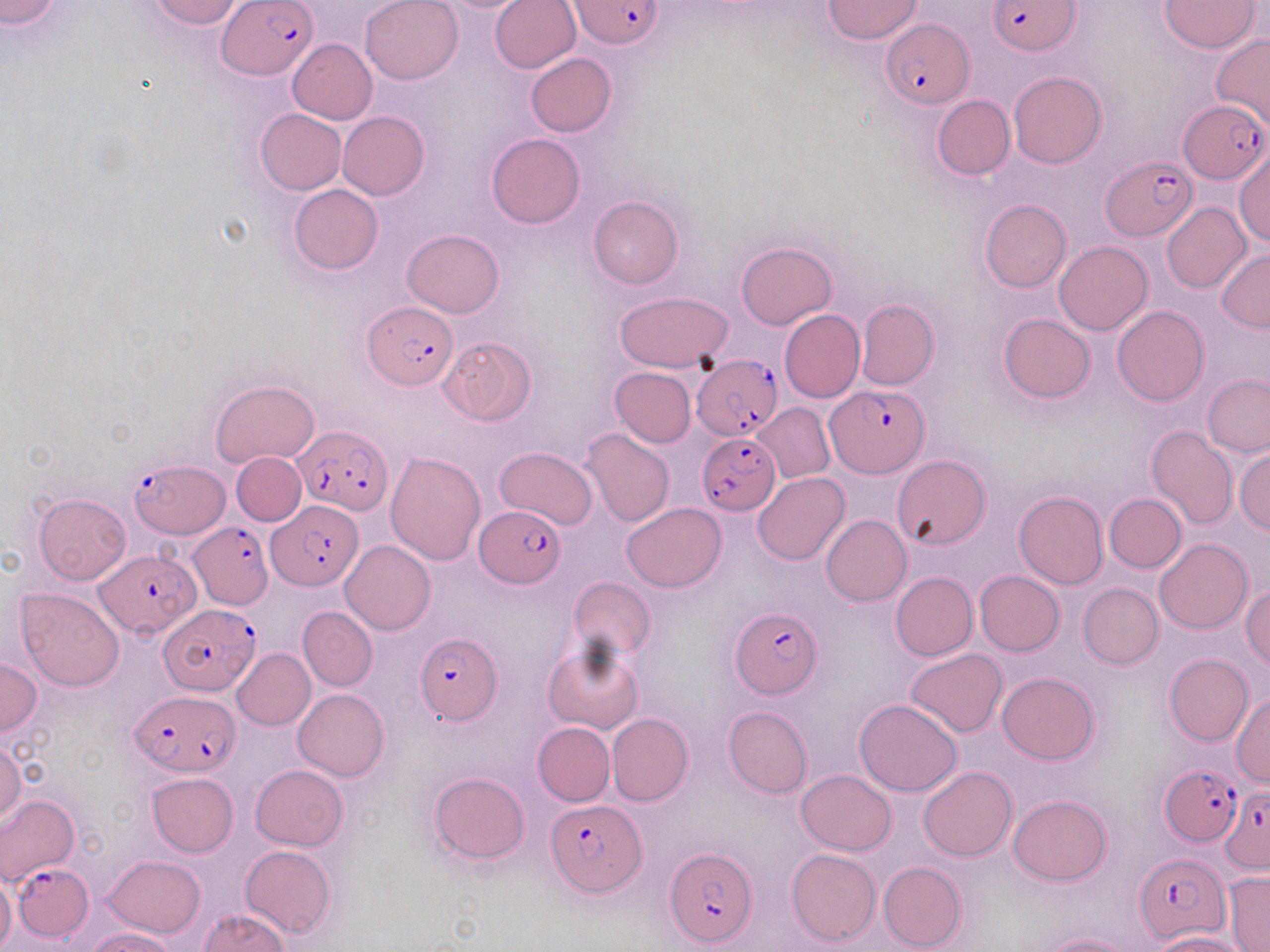
Summary:
  - Coordinate format: approximate bounding boxes as named x1/y1/x2/y2 corners in pixels
  - Uninfected red blood cell locations: (x1=0, y1=0, x2=61, y2=28), (x1=148, y1=0, x2=242, y2=28), (x1=359, y1=0, x2=463, y2=85), (x1=489, y1=0, x2=582, y2=73), (x1=823, y1=0, x2=922, y2=44), (x1=1160, y1=1, x2=1261, y2=52), (x1=1211, y1=33, x2=1270, y2=132), (x1=288, y1=39, x2=377, y2=122), (x1=525, y1=53, x2=616, y2=135), (x1=1009, y1=71, x2=1106, y2=168), (x1=932, y1=95, x2=1015, y2=180), (x1=256, y1=108, x2=347, y2=194), (x1=338, y1=111, x2=429, y2=199), (x1=487, y1=133, x2=584, y2=228), (x1=1235, y1=148, x2=1269, y2=244), (x1=288, y1=184, x2=383, y2=275), (x1=589, y1=195, x2=683, y2=289), (x1=980, y1=198, x2=1072, y2=292), (x1=1162, y1=203, x2=1251, y2=293), (x1=403, y1=229, x2=504, y2=317), (x1=736, y1=241, x2=836, y2=329), (x1=1055, y1=241, x2=1153, y2=336), (x1=1217, y1=248, x2=1270, y2=332), (x1=614, y1=291, x2=732, y2=372), (x1=856, y1=299, x2=939, y2=390), (x1=1112, y1=306, x2=1209, y2=406), (x1=778, y1=309, x2=865, y2=403), (x1=998, y1=313, x2=1094, y2=404), (x1=440, y1=336, x2=537, y2=424), (x1=609, y1=367, x2=697, y2=447), (x1=1203, y1=374, x2=1270, y2=456), (x1=211, y1=380, x2=318, y2=468), (x1=754, y1=404, x2=835, y2=483), (x1=1146, y1=425, x2=1238, y2=529), (x1=581, y1=428, x2=675, y2=529), (x1=494, y1=446, x2=598, y2=529), (x1=1234, y1=447, x2=1270, y2=534), (x1=386, y1=450, x2=487, y2=566), (x1=232, y1=452, x2=305, y2=526), (x1=894, y1=455, x2=989, y2=550), (x1=753, y1=473, x2=850, y2=565), (x1=1014, y1=489, x2=1108, y2=588), (x1=34, y1=493, x2=131, y2=585), (x1=1105, y1=493, x2=1186, y2=573), (x1=621, y1=502, x2=726, y2=591), (x1=821, y1=515, x2=911, y2=606), (x1=1154, y1=537, x2=1252, y2=634), (x1=340, y1=540, x2=434, y2=635), (x1=890, y1=570, x2=977, y2=661), (x1=975, y1=570, x2=1065, y2=656), (x1=569, y1=577, x2=655, y2=660), (x1=1078, y1=583, x2=1163, y2=669), (x1=1241, y1=585, x2=1270, y2=668), (x1=16, y1=586, x2=125, y2=692), (x1=298, y1=606, x2=378, y2=691), (x1=542, y1=638, x2=644, y2=735), (x1=233, y1=648, x2=315, y2=730), (x1=905, y1=649, x2=1007, y2=737), (x1=1164, y1=654, x2=1253, y2=747), (x1=0, y1=656, x2=41, y2=739), (x1=997, y1=672, x2=1099, y2=764), (x1=294, y1=689, x2=389, y2=781), (x1=1231, y1=694, x2=1270, y2=787), (x1=853, y1=698, x2=963, y2=797), (x1=723, y1=705, x2=813, y2=798), (x1=606, y1=714, x2=693, y2=806), (x1=533, y1=722, x2=614, y2=807), (x1=0, y1=740, x2=25, y2=829), (x1=251, y1=765, x2=348, y2=851), (x1=918, y1=766, x2=1017, y2=861), (x1=796, y1=769, x2=896, y2=855), (x1=429, y1=772, x2=529, y2=864), (x1=146, y1=773, x2=238, y2=857), (x1=0, y1=793, x2=79, y2=885), (x1=1008, y1=795, x2=1112, y2=885), (x1=240, y1=845, x2=337, y2=939), (x1=786, y1=848, x2=880, y2=946), (x1=104, y1=854, x2=205, y2=938), (x1=877, y1=861, x2=966, y2=950), (x1=1224, y1=871, x2=1270, y2=950), (x1=0, y1=875, x2=16, y2=951), (x1=201, y1=909, x2=289, y2=951), (x1=87, y1=928, x2=181, y2=952), (x1=1151, y1=931, x2=1250, y2=952), (x1=1037, y1=933, x2=1136, y2=952)
  - Plasmodium falciparum-infected red blood cell locations: (x1=221, y1=0, x2=317, y2=81), (x1=571, y1=0, x2=664, y2=50), (x1=989, y1=1, x2=1079, y2=54), (x1=882, y1=19, x2=972, y2=109), (x1=1178, y1=99, x2=1268, y2=183), (x1=1100, y1=155, x2=1197, y2=241), (x1=364, y1=301, x2=458, y2=389), (x1=691, y1=356, x2=782, y2=441), (x1=825, y1=385, x2=929, y2=478), (x1=294, y1=424, x2=393, y2=513), (x1=697, y1=432, x2=781, y2=516), (x1=130, y1=458, x2=227, y2=539), (x1=266, y1=504, x2=362, y2=591), (x1=475, y1=506, x2=563, y2=586), (x1=189, y1=522, x2=272, y2=607), (x1=95, y1=548, x2=200, y2=639), (x1=157, y1=605, x2=260, y2=695), (x1=730, y1=608, x2=820, y2=699), (x1=415, y1=631, x2=503, y2=726), (x1=131, y1=692, x2=239, y2=778), (x1=1160, y1=766, x2=1242, y2=845), (x1=1219, y1=786, x2=1269, y2=873), (x1=546, y1=801, x2=644, y2=896), (x1=665, y1=847, x2=757, y2=947), (x1=1135, y1=854, x2=1229, y2=943), (x1=15, y1=865, x2=93, y2=937)
  - Slide-level diagnosis: Plasmodium falciparum
  - Image size: 1270×952 pixels
  - Stain: May-Grünwald-Giemsa
  - Field of view: single
  - Magnification: 1000x
  - Preparation: thin blood smear
  - Modality: light microscopy